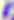 Photomicrograph. Toxoplasma gondii is seen. Captured at 400x magnification.